Locate every Plasmodium parasite.
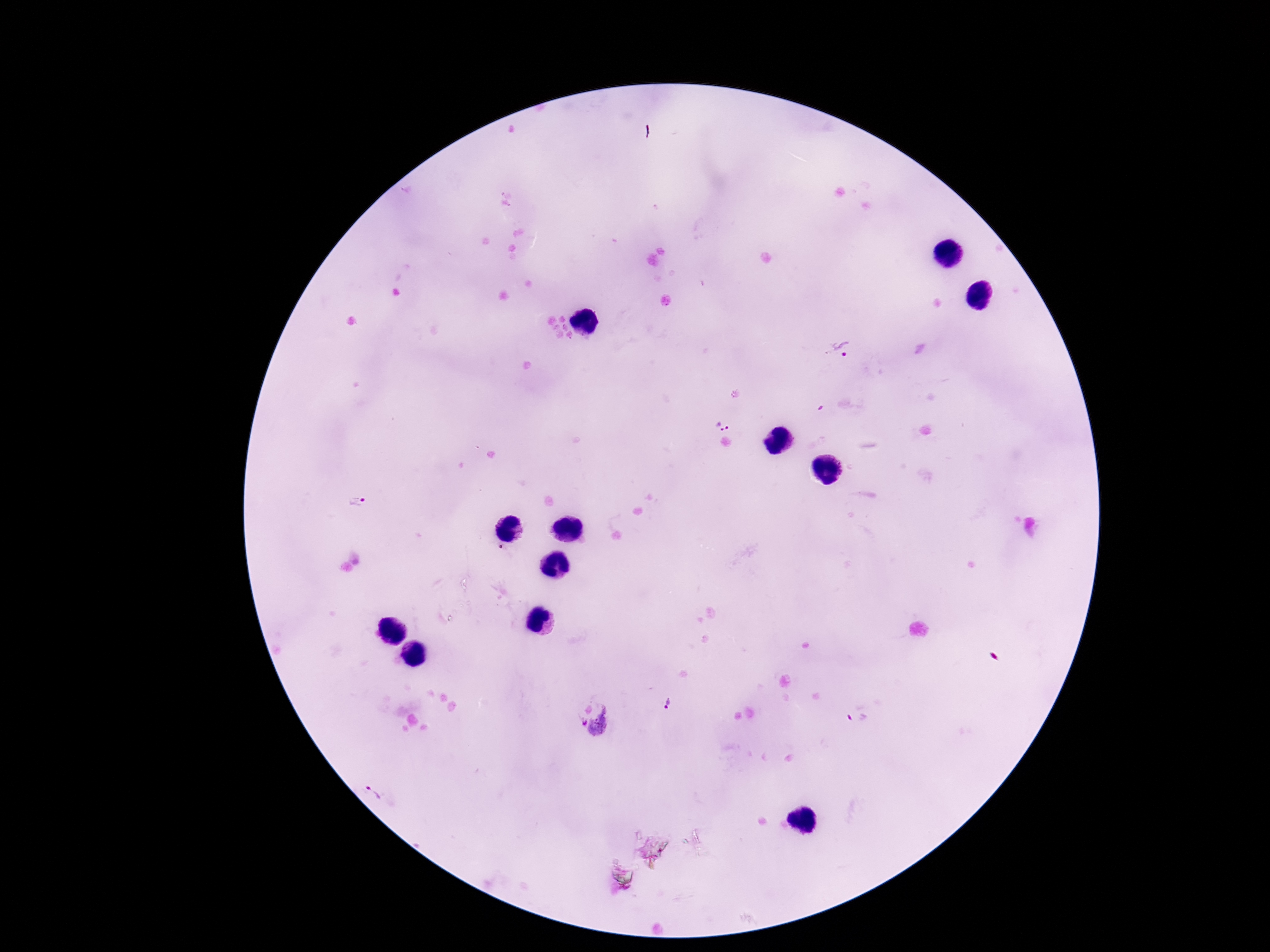
Approximate centers as (x, y) in pixels.
Plasmodium parasites: (841, 348), (722, 425), (357, 501), (503, 551), (670, 703), (856, 715), (592, 719), (377, 788).

{
  "patient_malaria_status": "positive",
  "capture": "smartphone camera through the microscope eyepiece",
  "magnification": "100x",
  "stain": "Giemsa",
  "preparation": "thick blood film",
  "field_of_view": "single",
  "image_size": "1270×952 pixels"
}